Assess the morphology of the erythrocytes.
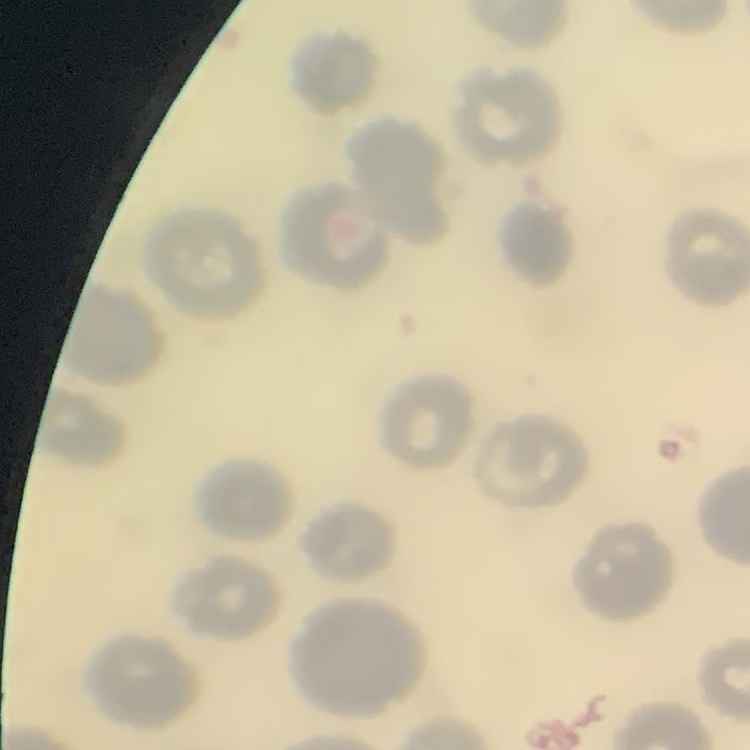

No rouleaux formation.

Summary:
  - Stain: Field's or Giemsa
  - Preparation: thin blood film
  - Image type: one tile cut from a larger photomicrograph